Classify this cell by malaria status.
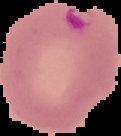

Parasitized.

image size = 121×136 pixels
preparation = thin blood film
image type = segmented cell region with the area outside set to black